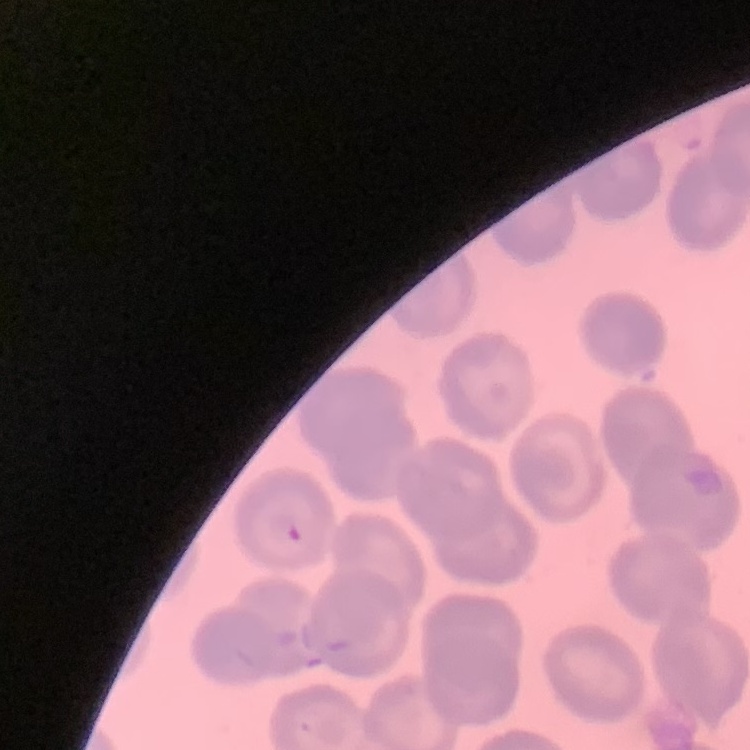

The erythrocytes show no rouleaux formation. One tile cut from a larger photomicrograph. Thin blood film. Field's or Giemsa stain.